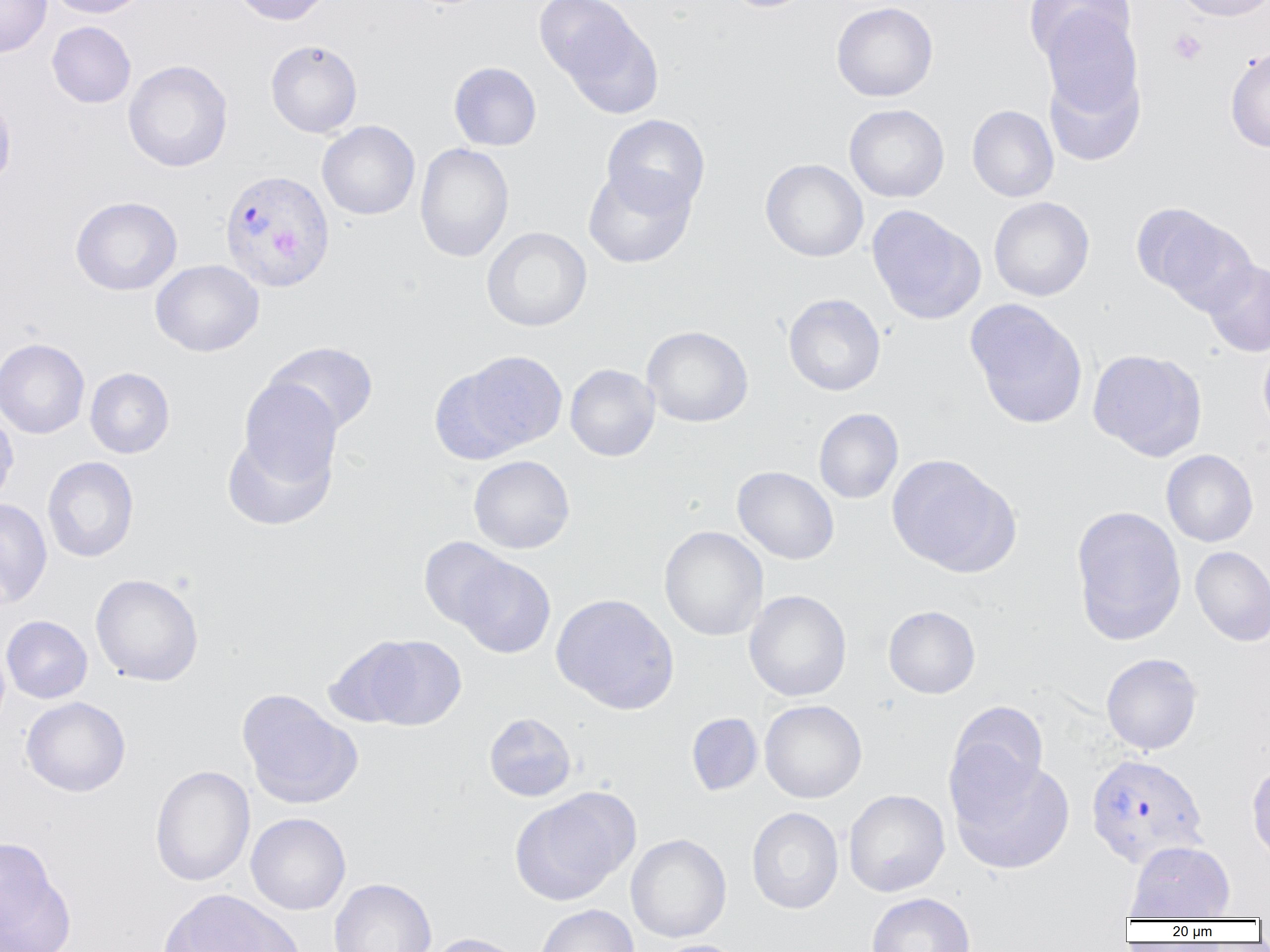
Approximate bounding boxes as [x1, y1, x2, y2] in pixels. Uninfected red blood cell locations: [0, 0, 52, 57], [45, 0, 150, 18], [229, 0, 334, 25], [538, 0, 662, 113], [719, 0, 817, 13], [1024, 0, 1137, 68], [1171, 0, 1270, 22], [831, 1, 938, 102], [1039, 9, 1143, 118], [47, 21, 136, 108], [265, 39, 363, 138], [1225, 46, 1270, 153], [122, 59, 234, 172], [448, 61, 542, 151], [1043, 61, 1146, 167], [0, 87, 16, 193], [844, 103, 949, 203], [967, 104, 1059, 202], [601, 114, 710, 214], [316, 120, 420, 220], [414, 143, 514, 262], [760, 158, 868, 262], [583, 166, 696, 268], [70, 196, 182, 296], [989, 197, 1094, 301], [1134, 203, 1257, 312], [866, 205, 986, 325], [481, 227, 592, 331], [150, 259, 264, 357], [1203, 259, 1270, 357], [783, 293, 886, 396], [965, 299, 1089, 429], [641, 325, 753, 427], [0, 337, 90, 439], [263, 341, 379, 436], [1258, 341, 1270, 438], [1088, 348, 1207, 460], [443, 351, 568, 458], [565, 364, 660, 461], [84, 367, 175, 458], [238, 379, 342, 489], [0, 407, 18, 509], [814, 408, 903, 504], [222, 429, 336, 529], [1161, 449, 1258, 547], [887, 454, 1019, 576], [468, 455, 575, 554], [41, 456, 139, 563], [733, 466, 839, 564], [0, 498, 52, 607], [1071, 505, 1186, 645], [659, 526, 768, 641], [418, 537, 515, 631], [1190, 545, 1270, 646], [453, 556, 556, 658], [90, 572, 204, 687], [744, 590, 852, 702], [551, 593, 679, 714], [883, 605, 980, 698], [1, 615, 93, 704], [348, 635, 467, 730], [1101, 652, 1203, 755], [237, 689, 362, 810], [21, 696, 131, 797], [759, 700, 867, 803], [946, 701, 1049, 815], [484, 712, 576, 802], [686, 713, 763, 796], [948, 755, 1075, 875], [1247, 760, 1270, 864], [149, 765, 255, 887], [510, 788, 639, 906], [844, 789, 950, 896], [746, 807, 844, 914], [245, 812, 351, 915], [625, 833, 732, 942], [0, 837, 72, 952], [1125, 840, 1235, 920], [329, 877, 437, 952], [866, 892, 976, 952], [156, 896, 302, 949], [534, 904, 639, 952], [425, 932, 529, 952], [651, 939, 746, 952]. Plasmodium vivax-infected red blood cell locations: [218, 169, 335, 292], [1085, 753, 1209, 869]. Platelet locations: [1168, 28, 1208, 66]. Slide-level diagnosis: Plasmodium vivax. Thin blood film. Captured at 1000x magnification. Image is 1270×952 pixels. One field of a larger specimen. Light microscopy.